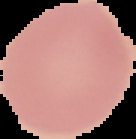

Image is 136×139 pixels. From a thin blood smear. The area outside the segmented cell region is set to black. Result: no malaria parasites detected.